Comment on the morphology of the red blood cells.
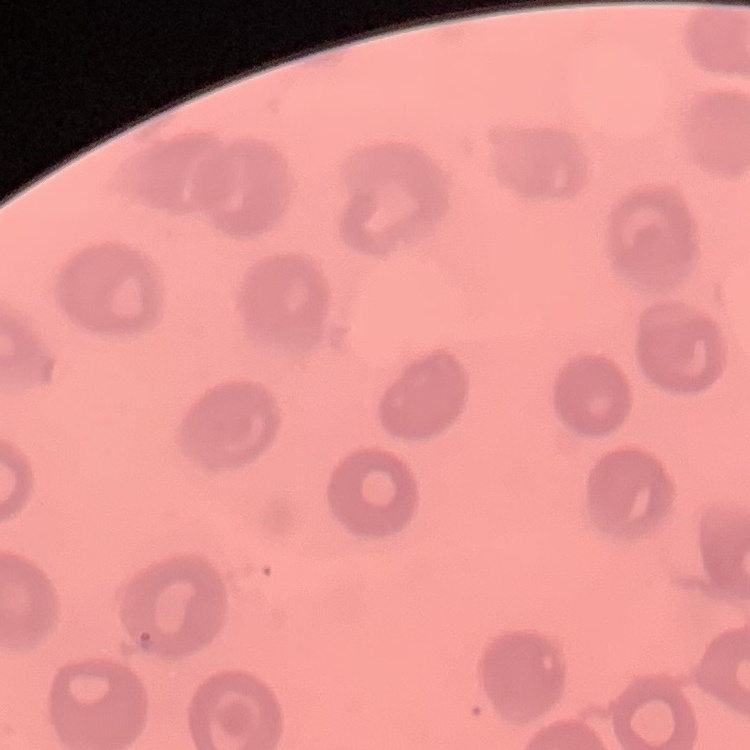

No rouleaux formation.

{
  "preparation": "thin blood smear",
  "stain": "Field's or Giemsa",
  "image_type": "square crop of a larger photomicrograph"
}